Assess the background quality.
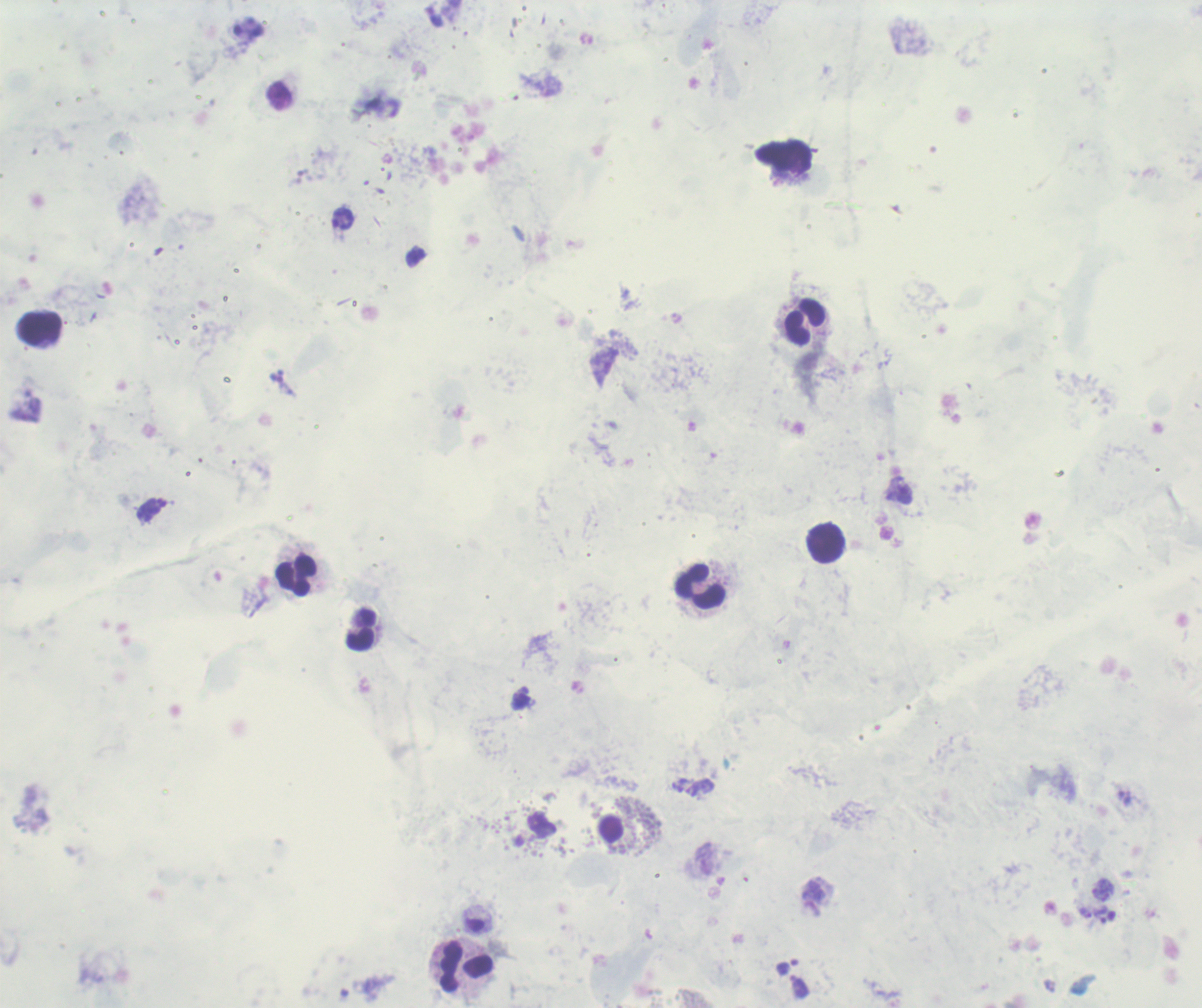
Poor.

coordinate format = approximate centers as [x, y] in pixels
trophozoite locations = [902, 489], [1086, 913], [1101, 914]
leukocyte locations = [803, 322], [40, 329], [826, 544], [295, 576], [701, 588], [361, 630], [466, 966]
preparation = thick smear of blood
image size = 1202×1008 pixels
context = previously used in a real diagnosis
field of view = one from this slide
result = Plasmodium parasites identified
stain = Romanowsky
magnification = 100x